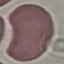
Malaria status: uninfected. Acquired by smartphone through the microscope eyepiece. Giemsa-stained preparation. Automatically extracted cell patch, resized to 64 × 64 pixels. Thin smear of blood.